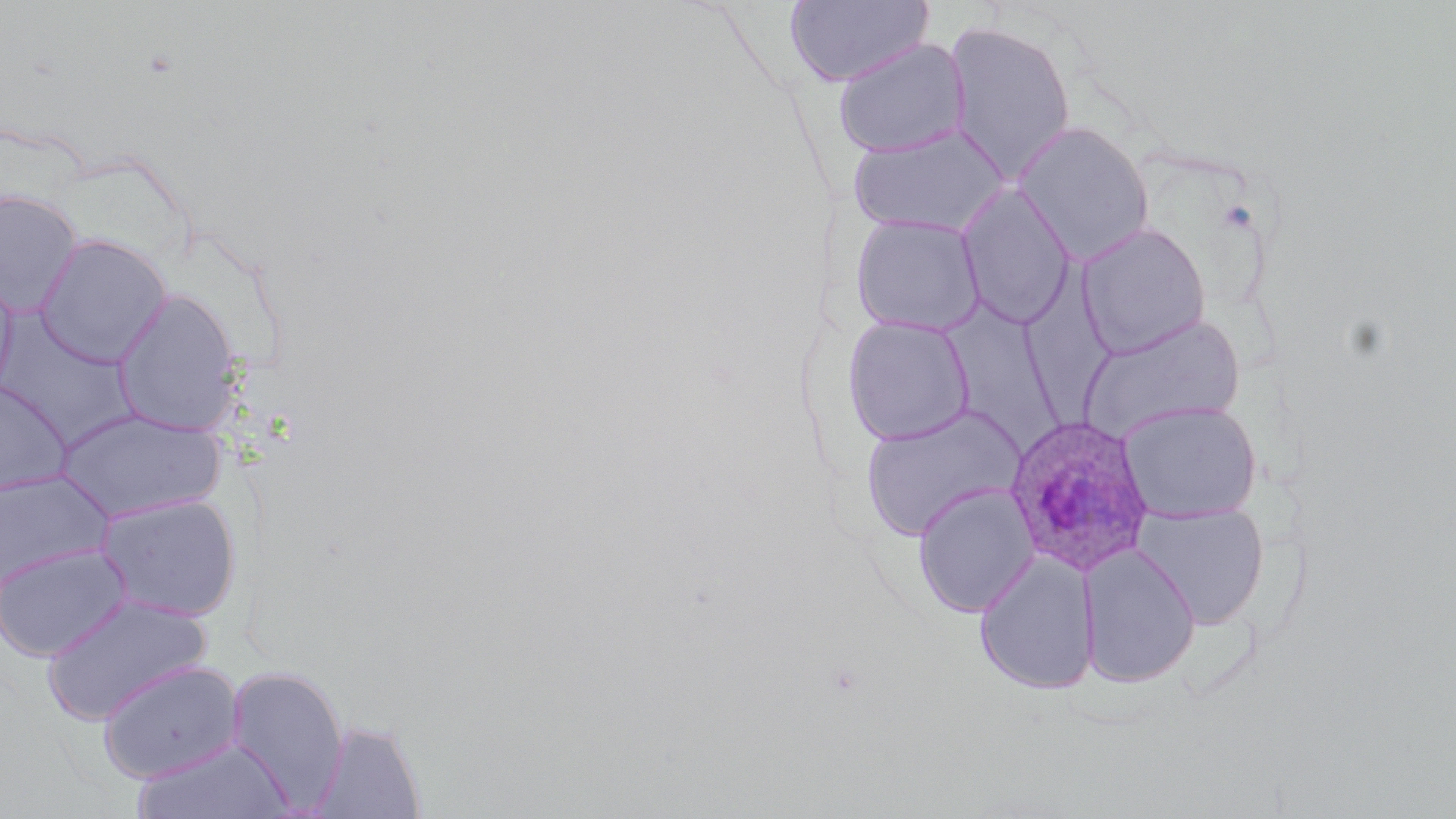

Summary:
  - Coordinate format: approximate bounding boxes as (x1, y1, x2, y2) in pixels
  - Plasmodium ovale-infected red blood cell locations: (1003, 414, 1156, 577)
  - Uninfected red blood cell locations: (784, 0, 934, 88), (942, 21, 1077, 184), (833, 37, 971, 159), (1013, 121, 1155, 264), (847, 124, 1009, 237), (956, 183, 1075, 330), (0, 189, 83, 317), (850, 214, 986, 337), (1076, 222, 1211, 359), (34, 233, 171, 368), (1022, 250, 1119, 431), (0, 264, 18, 399), (111, 287, 244, 437), (946, 293, 1068, 458), (0, 312, 140, 452), (1076, 313, 1246, 441), (842, 314, 976, 447), (0, 379, 72, 496), (1117, 400, 1262, 523), (858, 404, 1026, 541), (55, 408, 226, 523), (0, 470, 114, 590), (912, 483, 1039, 618), (95, 493, 243, 621), (1133, 501, 1268, 628), (0, 542, 132, 662), (1079, 543, 1201, 688), (974, 551, 1100, 695), (40, 593, 211, 725), (96, 659, 245, 783), (224, 665, 350, 812), (309, 719, 427, 818), (130, 736, 297, 819)
  - Slide-level diagnosis: Plasmodium ovale
  - Modality: light microscopy
  - Field of view: one of a larger specimen
  - Magnification: 1000x
  - Image size: 1456×819 pixels
  - Stain: May-Grünwald-Giemsa
  - Preparation: thin blood smear